Locate and identify every blood parasite.
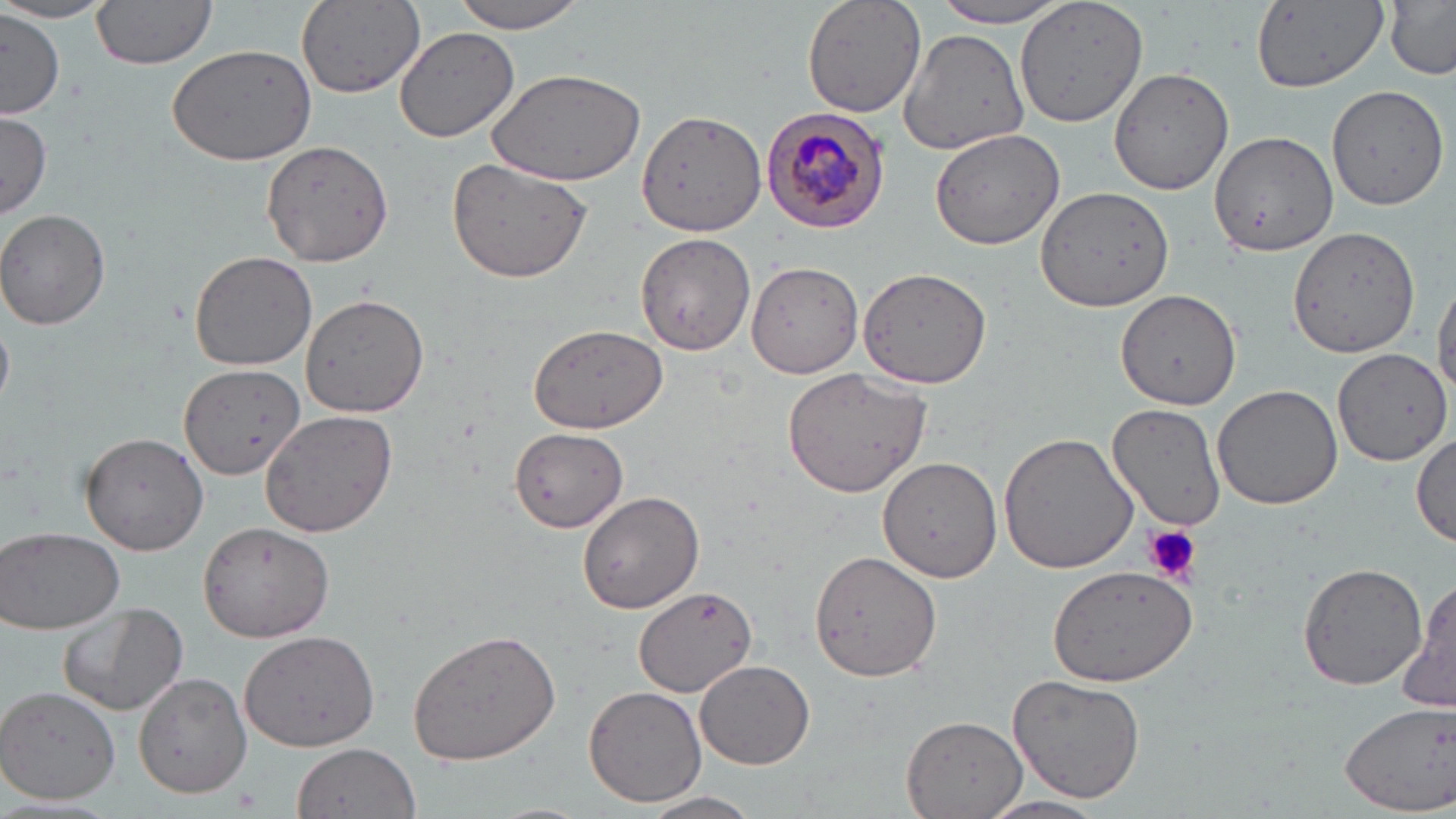

Approximate bounding boxes as (x1,y1)-(x2,y2) corner pairs in pixels.
Plasmodium malariae-infected red blood cells: (760,108)-(891,233).
No Plasmodium falciparum, Plasmodium ovale, Plasmodium vivax, Babesia divergens, or Trypanosoma brucei observed.

slide-level diagnosis = Plasmodium malariae
magnification = 1000x
image size = 1456×819 pixels
field of view = single
modality = light microscopy
uninfected red blood cell locations = approximate bounding boxes as (x1,y1)-(x2,y2) corner pairs in pixels: (91,0)-(218,69), (296,0)-(425,100), (450,0)-(592,34), (802,0)-(927,118), (930,0)-(1078,29), (0,1)-(118,25), (1016,1)-(1148,128), (1249,1)-(1389,91), (1385,2)-(1456,79), (0,10)-(65,116), (394,27)-(520,143), (898,28)-(1032,155), (166,43)-(317,166), (1110,67)-(1234,194), (483,68)-(646,185), (1327,83)-(1450,210), (636,109)-(768,240), (0,112)-(51,219), (929,129)-(1065,249), (1210,131)-(1339,259), (261,139)-(394,266), (448,154)-(592,283), (1036,185)-(1174,312), (0,211)-(110,329), (1290,225)-(1420,357), (636,232)-(757,356), (189,250)-(318,372), (748,262)-(865,379), (857,266)-(992,391), (1432,273)-(1456,406), (1115,288)-(1242,409), (299,292)-(429,418), (0,317)-(13,407), (527,324)-(669,433), (1332,346)-(1452,466), (180,364)-(307,480), (781,367)-(932,500), (1211,382)-(1345,510), (1107,403)-(1227,532), (258,410)-(398,539), (509,425)-(630,533), (80,431)-(210,556), (998,432)-(1138,576), (1412,432)-(1455,548), (879,457)-(1002,583), (577,491)-(705,613), (197,520)-(334,643), (1,526)-(126,635), (808,549)-(944,682), (1045,562)-(1200,685), (1298,563)-(1426,690), (1398,577)-(1456,717), (636,583)-(765,702), (59,602)-(188,717), (406,629)-(562,766), (238,630)-(381,753), (694,657)-(817,769), (135,669)-(252,797), (1007,673)-(1147,804), (584,686)-(706,805), (0,688)-(120,802), (1340,703)-(1456,814), (902,714)-(1029,819), (291,743)-(424,819), (640,790)-(764,819), (975,795)-(1114,818)
preparation = thin blood film
platelet locations = approximate bounding boxes as (x1,y1)-(x2,y2) corner pairs in pixels: (1144,525)-(1202,586)
stain = May-Grünwald-Giemsa